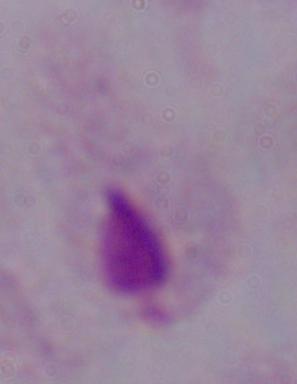

A trichomonad is shown. 1000x magnification. Micrograph.